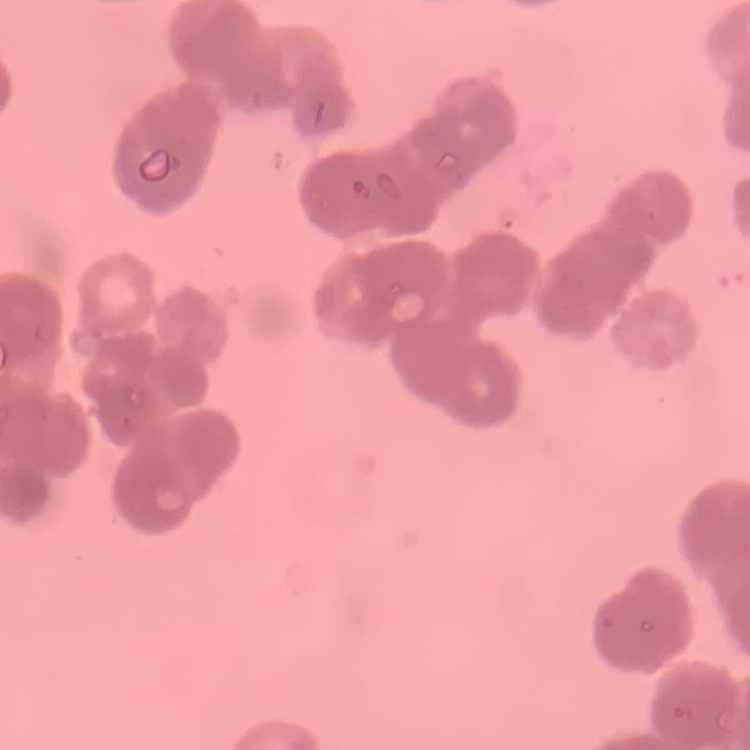
The erythrocytes show rouleaux formation. One tile cut from a larger photomicrograph. Thin peripheral smear. Field's or Giemsa stain.